Locate every blood parasite and identify its species.
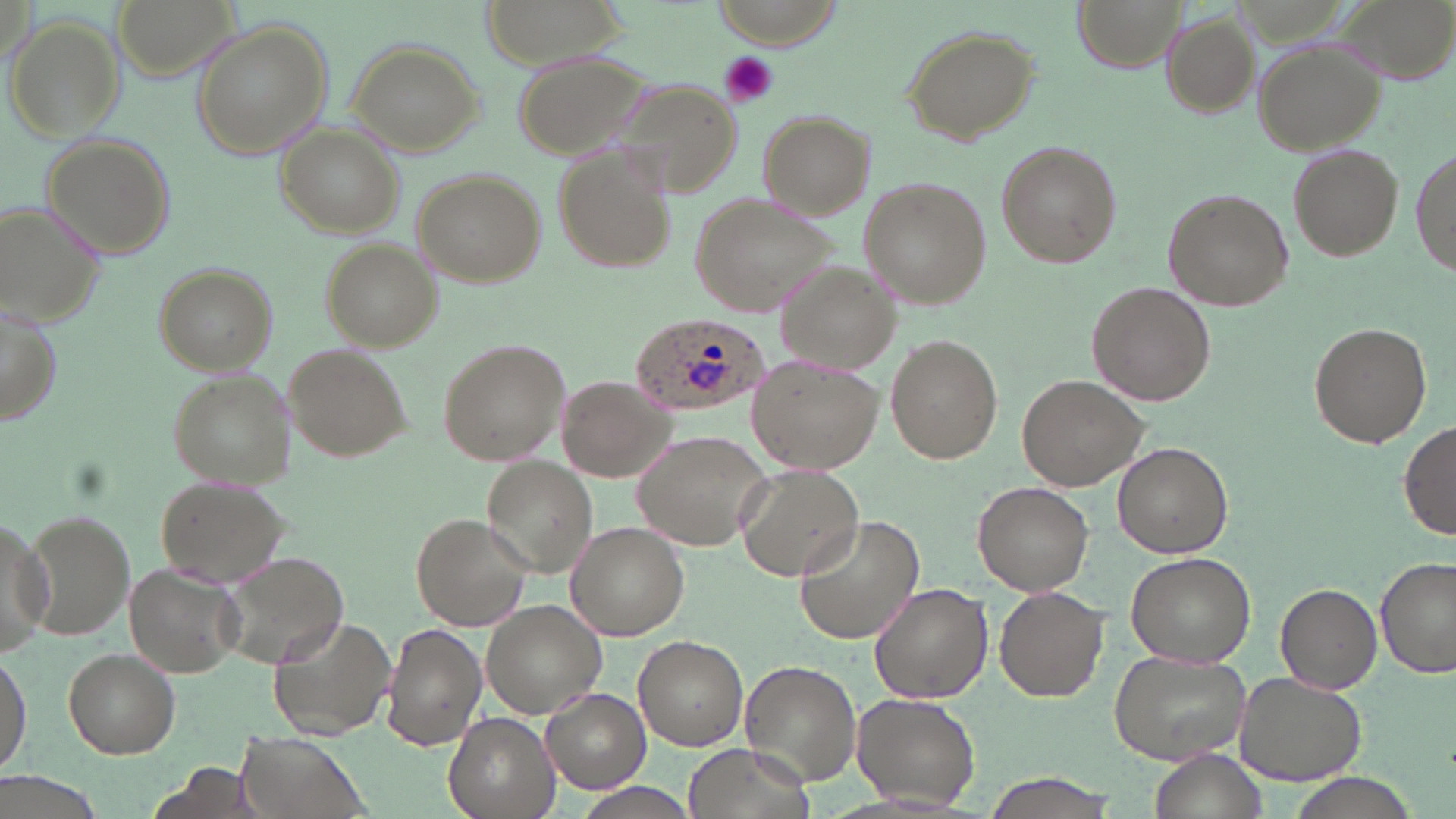

Approximate bounding boxes as (x1,y1)-(x2,y2) corner pairs in pixels.
Plasmodium ovale-infected red blood cells: (627,311)-(767,416).
No Plasmodium falciparum, Plasmodium malariae, Plasmodium vivax, Babesia divergens, or Trypanosoma brucei observed.

Uninfected red blood cell locations: (111,0)-(239,78), (482,0)-(629,64), (716,0)-(839,49), (1072,0)-(1186,71), (1163,13)-(1259,117), (7,17)-(124,140), (190,21)-(336,159), (903,25)-(1042,145), (1251,35)-(1388,155), (346,39)-(485,155), (514,49)-(654,159), (613,79)-(737,196), (757,111)-(875,219), (278,124)-(404,237), (39,133)-(178,259), (1413,141)-(1454,285), (996,142)-(1121,268), (1288,143)-(1405,259), (553,144)-(676,275), (413,169)-(548,288), (858,176)-(989,306), (1164,189)-(1289,311), (688,191)-(842,318), (0,201)-(108,327), (322,241)-(442,350), (775,260)-(903,377), (153,261)-(279,374), (1087,282)-(1215,405), (1,303)-(64,427), (1309,321)-(1432,449), (885,334)-(1003,464), (434,336)-(569,468), (285,345)-(410,461), (748,353)-(886,473), (167,370)-(297,488), (555,375)-(677,482), (1016,375)-(1144,491), (1399,420)-(1456,541), (634,428)-(775,550), (1113,441)-(1234,559), (482,457)-(597,577), (733,464)-(866,582), (156,476)-(292,585), (972,481)-(1094,595), (21,509)-(139,642), (412,513)-(534,632), (0,514)-(53,657), (792,515)-(926,647), (567,522)-(689,641), (216,551)-(350,669), (1126,553)-(1259,668), (1376,557)-(1455,680), (123,562)-(244,678), (869,581)-(993,703), (1275,582)-(1382,693), (994,585)-(1108,702), (481,599)-(606,717), (268,613)-(399,741), (380,622)-(486,753), (633,636)-(748,750), (0,647)-(33,777), (62,648)-(180,757), (1108,649)-(1252,766), (740,660)-(862,786), (1234,674)-(1365,785), (541,689)-(651,794), (850,691)-(983,812), (444,710)-(560,819), (235,734)-(367,819), (684,744)-(805,819), (1151,750)-(1266,819), (151,761)-(262,819), (977,772)-(1114,817), (575,784)-(697,818). Platelet locations: (718,50)-(778,106). Slide-level diagnosis: Plasmodium ovale. May-Grünwald-Giemsa-stained preparation. 1000x magnification. Image is 1456×819 pixels. Light microscopy. Single field of view. Thin blood smear.